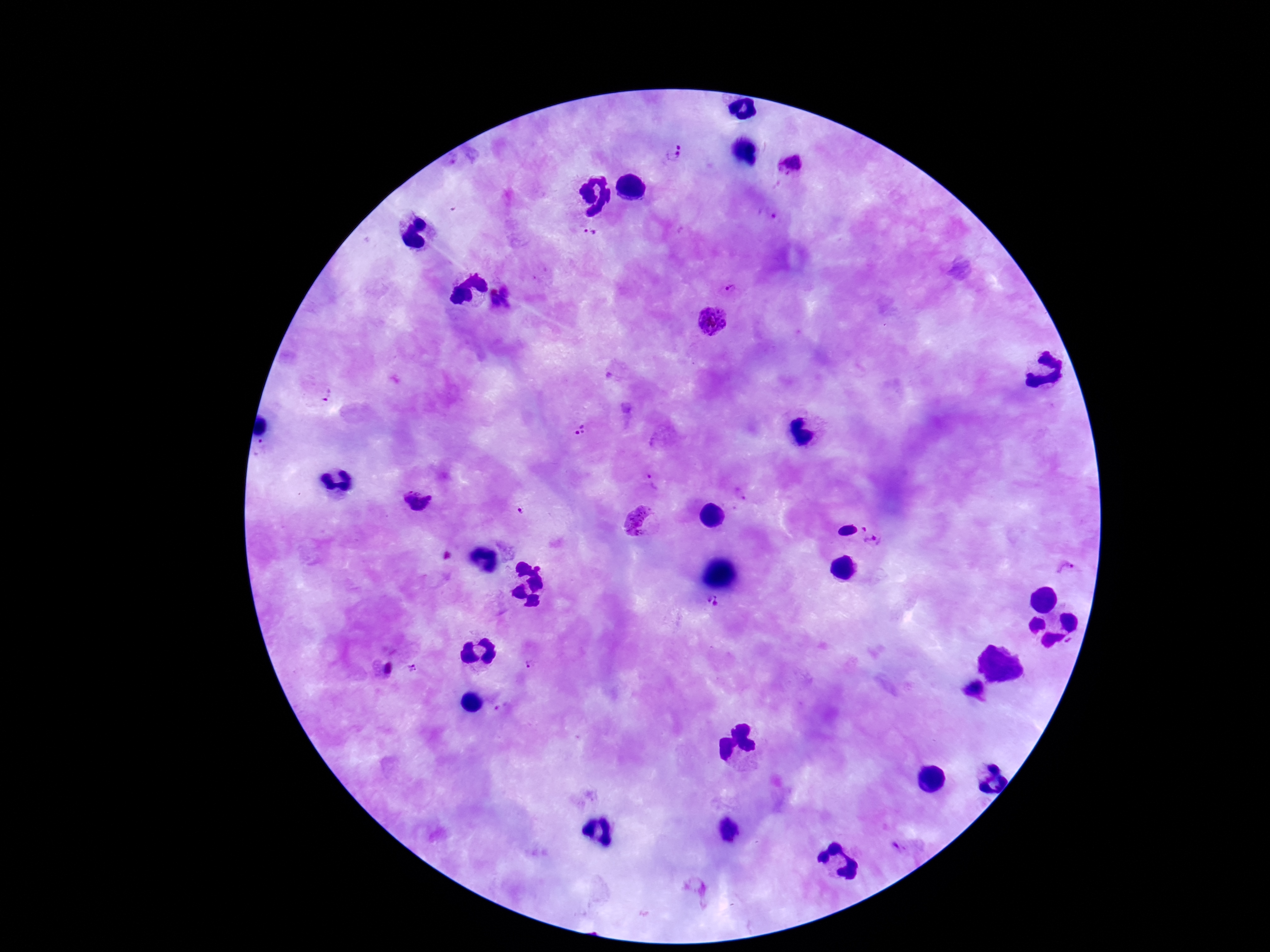 Approximate centers as {x, y} in pixels. Plasmodium parasite locations: {674, 155}, {792, 165}, {767, 218}, {591, 237}, {732, 284}, {716, 320}, {325, 397}, {579, 429}, {653, 484}, {417, 502}, {520, 512}, {639, 523}, {844, 524}, {877, 545}, {1063, 569}, {714, 603}, {531, 666}, {415, 667}, {386, 669}, {976, 693}. Patient malaria status: infected. Photographed through the microscope eyepiece with a smartphone camera. 100x magnification. Giemsa stain. Single field of view. Image is 1270×952 pixels. Thick blood film.